Identify the parasite.
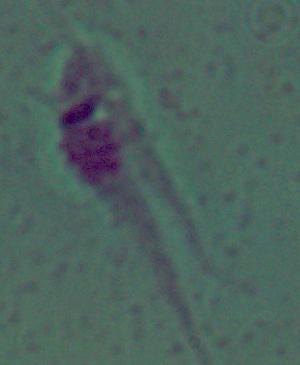

This is Leishmania.

Summary:
  - Modality: micrograph
  - Magnification: 1000x